Describe the morphology of the erythrocytes.
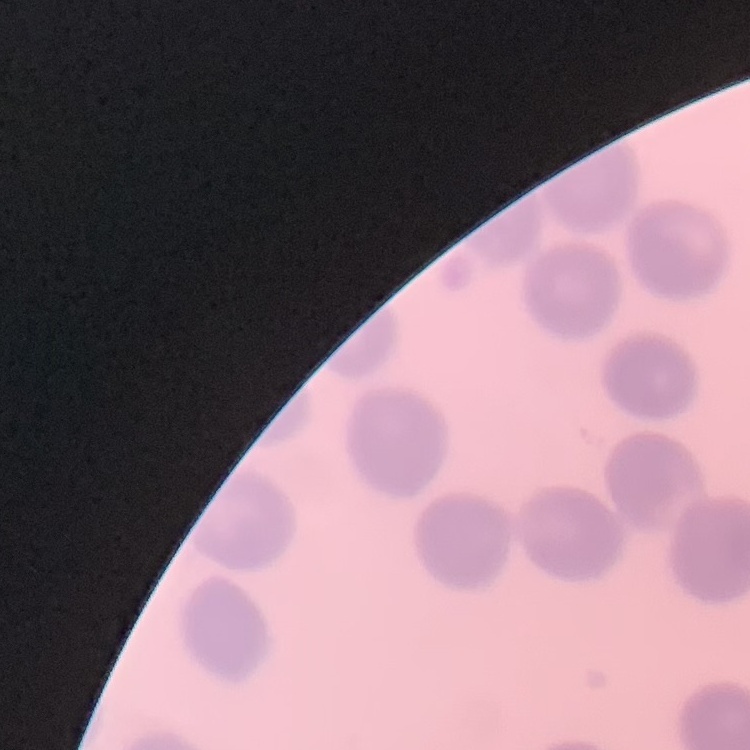

They show no rouleaux formation.

One tile cut from a larger photomicrograph. Stained with either Field's or Giemsa. Thin peripheral smear.